Identify the parasite.
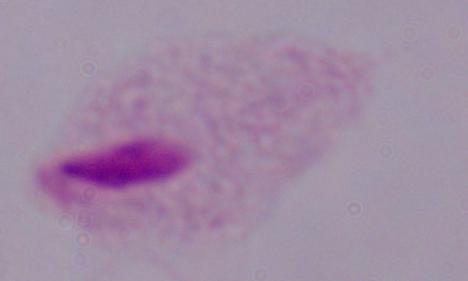

A trichomonad.

{
  "modality": "micrograph",
  "magnification": "1000x"
}